State the blood parasite species.
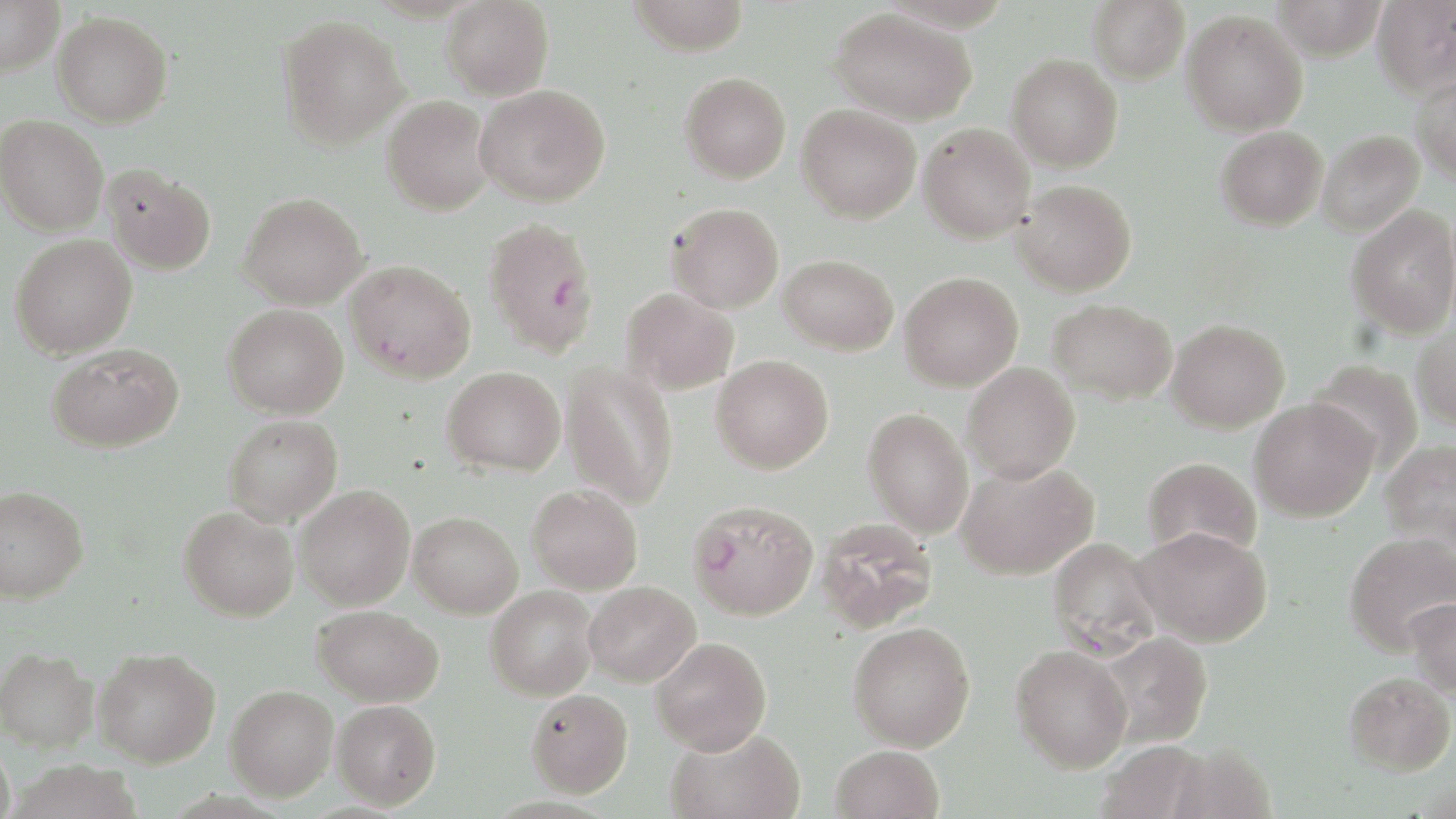
Plasmodium falciparum.

Approximate bounding boxes as [x1, y1, x2, y2] in pixels. Plasmodium falciparum-infected red blood cell locations: [489, 227, 601, 359], [345, 260, 476, 383], [686, 499, 819, 620]. Uninfected red blood cell locations: [441, 0, 554, 101], [627, 0, 750, 55], [1087, 0, 1190, 84], [1271, 0, 1388, 61], [1372, 0, 1456, 98], [0, 1, 64, 76], [830, 7, 977, 125], [1181, 10, 1308, 136], [52, 11, 173, 127], [276, 14, 411, 151], [1007, 54, 1123, 172], [679, 71, 791, 184], [1411, 74, 1456, 186], [475, 83, 609, 208], [381, 94, 493, 215], [796, 104, 921, 223], [0, 115, 108, 236], [918, 123, 1035, 243], [1215, 125, 1328, 231], [1318, 130, 1425, 237], [103, 164, 216, 274], [1013, 179, 1137, 296], [238, 192, 368, 309], [666, 202, 784, 313], [1345, 204, 1456, 339], [9, 233, 137, 359], [778, 254, 898, 355], [899, 272, 1023, 391], [621, 288, 739, 395], [1048, 298, 1177, 404], [223, 303, 348, 419], [1166, 319, 1290, 433], [1411, 321, 1456, 430], [47, 344, 183, 453], [711, 355, 834, 474], [1307, 359, 1424, 473], [961, 362, 1080, 483], [561, 363, 678, 509], [442, 365, 565, 476], [1248, 397, 1378, 521], [863, 408, 974, 538], [224, 414, 342, 526], [1380, 439, 1456, 554], [1142, 457, 1262, 562], [956, 460, 1098, 580], [295, 484, 415, 609], [527, 484, 643, 594], [0, 485, 89, 603], [178, 506, 298, 621], [408, 511, 523, 618], [815, 518, 938, 634], [1132, 525, 1272, 646], [1344, 532, 1456, 655], [1047, 538, 1162, 659], [584, 582, 701, 687], [485, 585, 599, 700], [1405, 597, 1456, 698], [312, 604, 444, 706], [848, 622, 975, 751], [1096, 632, 1212, 748], [651, 637, 772, 754], [1011, 644, 1132, 772], [0, 647, 99, 753], [94, 647, 220, 767], [1343, 671, 1455, 776], [225, 684, 338, 801], [525, 688, 633, 798], [332, 699, 441, 810], [665, 727, 805, 819], [0, 737, 16, 819], [1096, 741, 1210, 819], [1164, 742, 1277, 819], [830, 744, 944, 819]. Optical microscopy. Captured at 1000x magnification. Thin blood smear. May-Grünwald-Giemsa-stained preparation. Single field of view. Image is 1456×819 pixels.